State the blood parasite species.
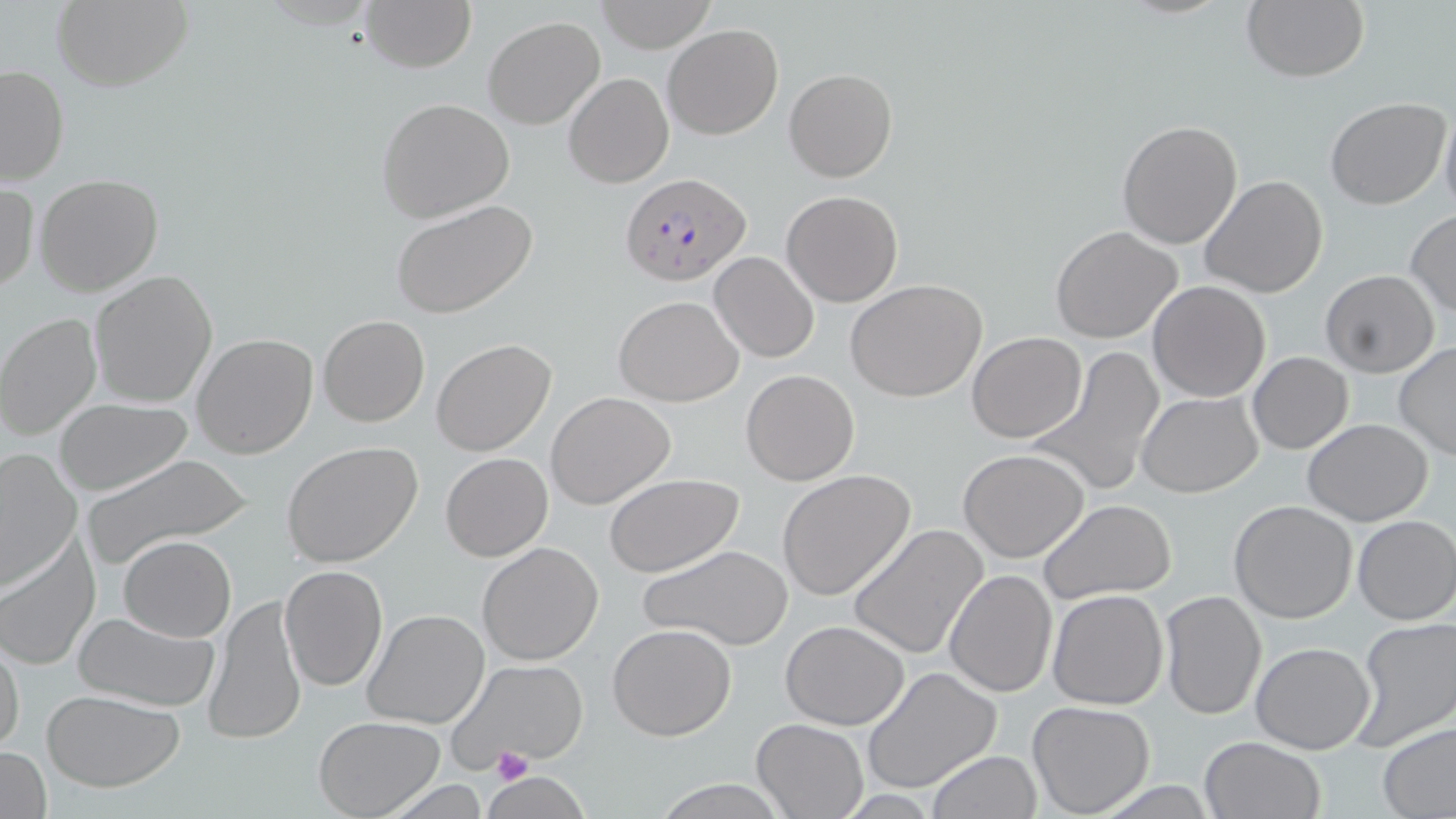
Plasmodium falciparum.

image size = 1456×819 pixels
stain = May-Grünwald-Giemsa
field of view = one of a larger specimen
modality = light microscopy
platelet locations = approximate bounding boxes as (x1,y1)-(x2,y2) corner pairs in pixels: (492,746)-(532,785)
preparation = thin blood smear
Plasmodium falciparum-infected red blood cell locations = approximate bounding boxes as (x1,y1)-(x2,y2) corner pairs in pixels: (621,173)-(750,285)
magnification = 1000x
uninfected red blood cell locations = approximate bounding boxes as (x1,y1)-(x2,y2) corner pairs in pixels: (51,0)-(191,91), (359,0)-(476,72), (1240,0)-(1369,83), (594,1)-(716,53), (482,16)-(604,130), (662,24)-(783,140), (0,63)-(68,187), (784,67)-(898,183), (563,73)-(673,189), (1324,96)-(1450,210), (376,98)-(516,222), (1440,106)-(1456,223), (1115,119)-(1243,250), (34,174)-(162,296), (1199,174)-(1330,299), (1,182)-(38,295), (781,190)-(902,307), (389,199)-(539,319), (1404,211)-(1456,320), (1049,226)-(1185,345), (709,252)-(819,363), (1319,270)-(1439,377), (88,271)-(219,408), (845,279)-(990,404), (1148,281)-(1271,402), (613,295)-(745,406), (0,312)-(102,440), (317,315)-(429,426), (966,331)-(1088,442), (192,333)-(319,460), (432,338)-(557,457), (1394,344)-(1456,461), (1029,346)-(1166,498), (1246,352)-(1354,454), (741,369)-(859,486), (1136,390)-(1263,496), (545,391)-(677,510), (54,398)-(192,495), (1303,419)-(1434,526), (282,442)-(424,569), (0,448)-(81,591), (957,448)-(1091,563), (81,453)-(253,567), (440,453)-(553,562), (777,469)-(915,600), (606,474)-(745,578), (1229,499)-(1359,623), (1038,500)-(1177,604), (1351,514)-(1456,626), (848,523)-(991,662), (119,535)-(236,641), (0,536)-(100,672), (476,541)-(605,666), (640,544)-(794,651), (279,564)-(388,692), (944,568)-(1058,697), (1046,589)-(1169,711), (1160,589)-(1266,720), (202,596)-(306,745), (363,608)-(492,730), (73,610)-(222,711), (1350,618)-(1456,749), (780,620)-(911,730), (608,623)-(737,741), (0,639)-(24,757), (1250,641)-(1377,754), (450,658)-(591,770), (862,665)-(1004,794), (41,689)-(186,792), (1027,699)-(1156,818), (314,716)-(444,818), (751,717)-(868,817), (1377,721)-(1456,817), (1198,735)-(1326,819), (1,746)-(51,819), (926,750)-(1042,819), (486,770)-(582,819), (647,775)-(788,818)